Identify the preparation type.
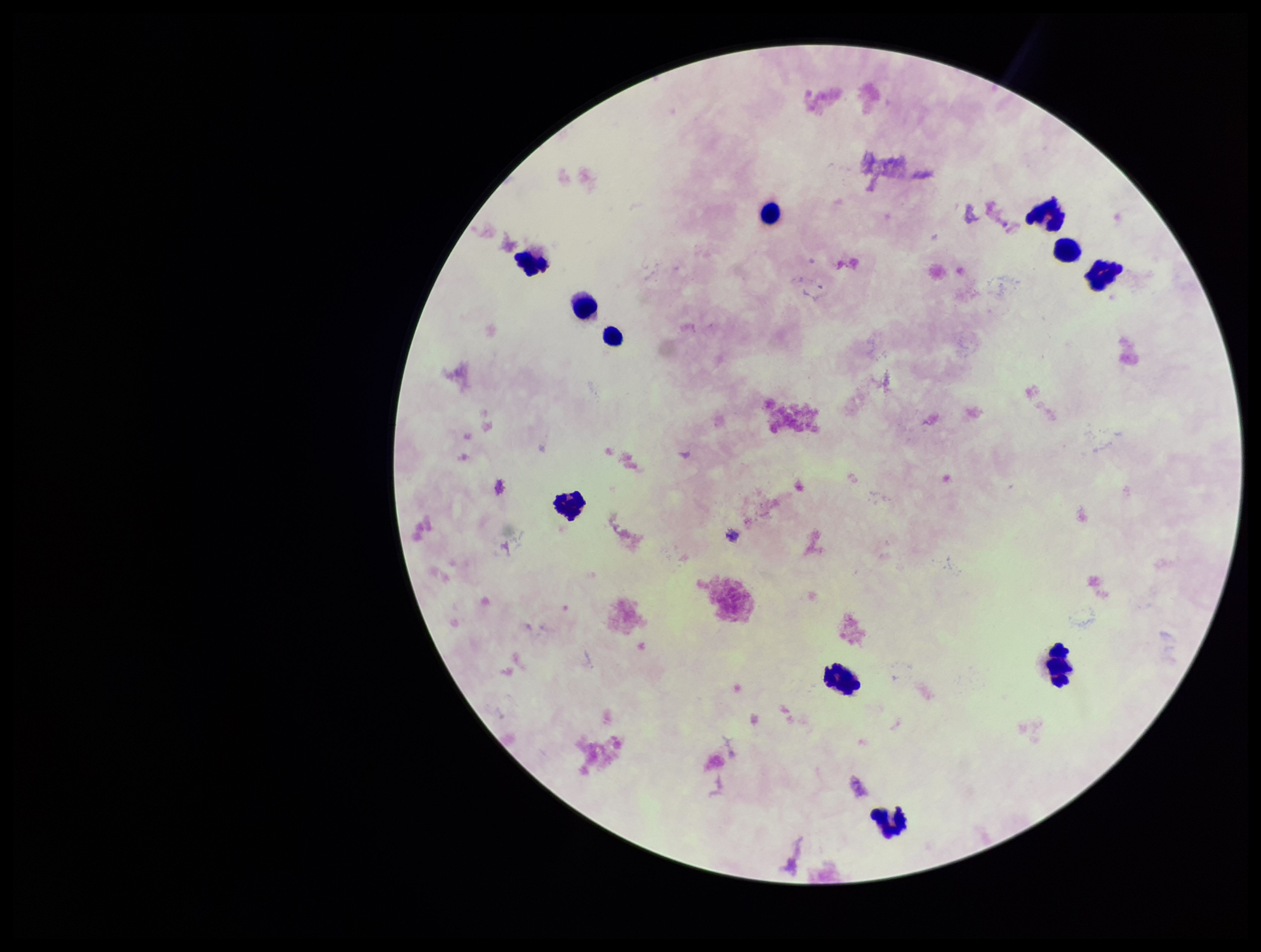
Thick.

parasite count = 0
image size = 1261×952 pixels
leukocyte count = 11
Plasmodium parasites = none identified
patient malaria status = negative
stain = Giemsa
capture = smartphone photograph through the microscope eyepiece
field of view = single